State which cell type is depicted.
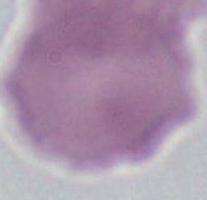
An erythrocyte.

Summary:
  - Modality: photomicrograph
  - Magnification: 1000x